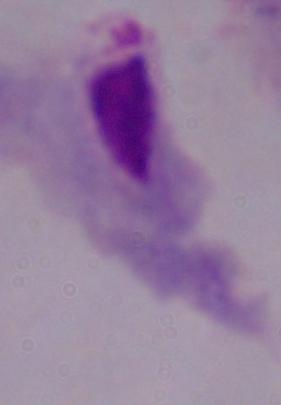

Photomicrograph. 1000x magnification. A trichomonad is shown.